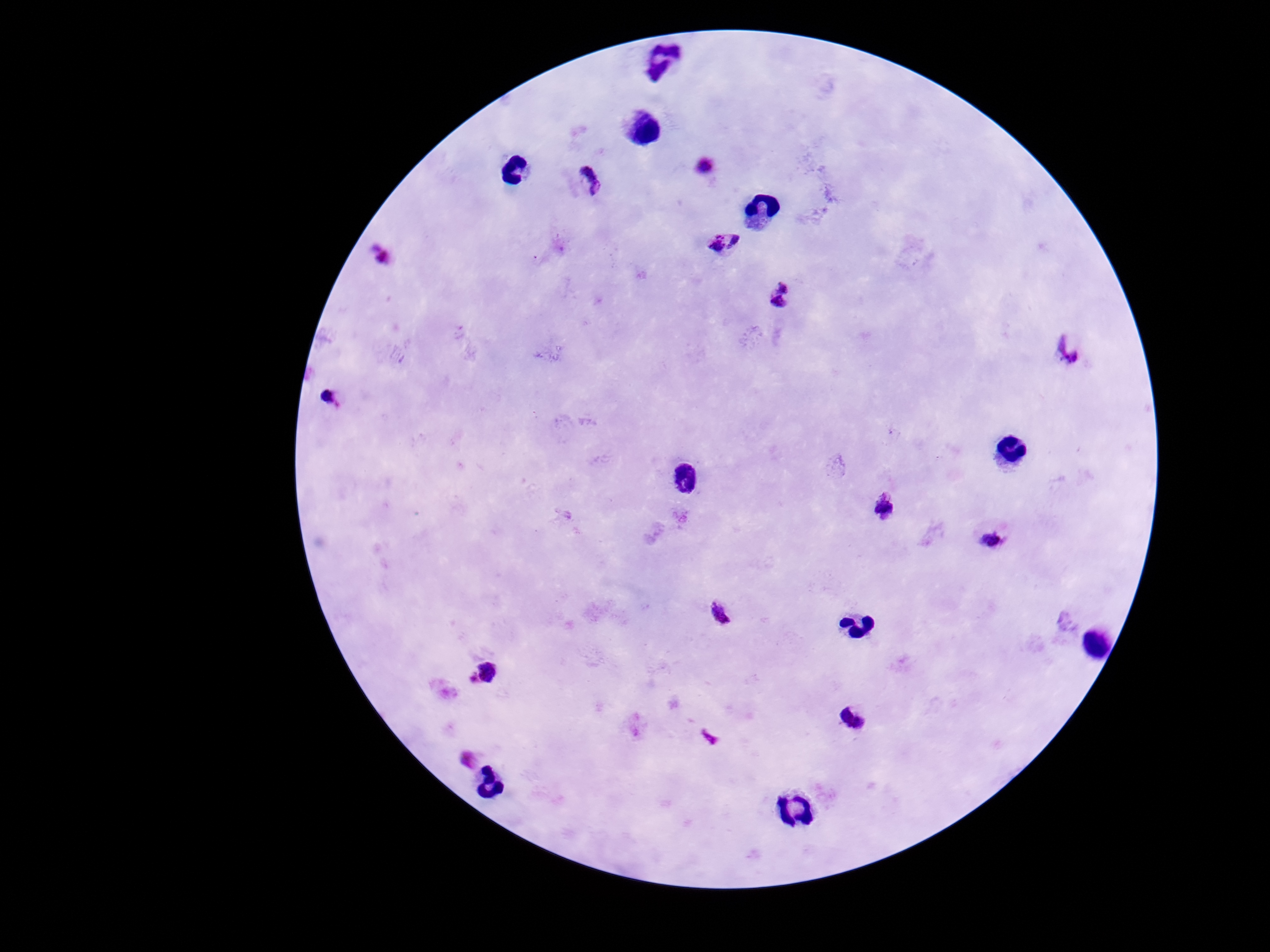
Approximate centers as (x, y) in pixels.
Summary:
  - Plasmodium parasite locations: (590, 180), (724, 244), (781, 294), (1069, 348), (332, 397), (683, 478), (886, 507), (996, 538), (719, 613), (487, 671), (855, 717)
  - Magnification: 100x
  - Preparation: thick peripheral-blood smear
  - Field of view: single
  - Image size: 1270×952 pixels
  - Patient malaria status: positive
  - Stain: Giemsa
  - Capture: smartphone camera through the microscope eyepiece